Locate every Plasmodium falciparum-infected red blood cell.
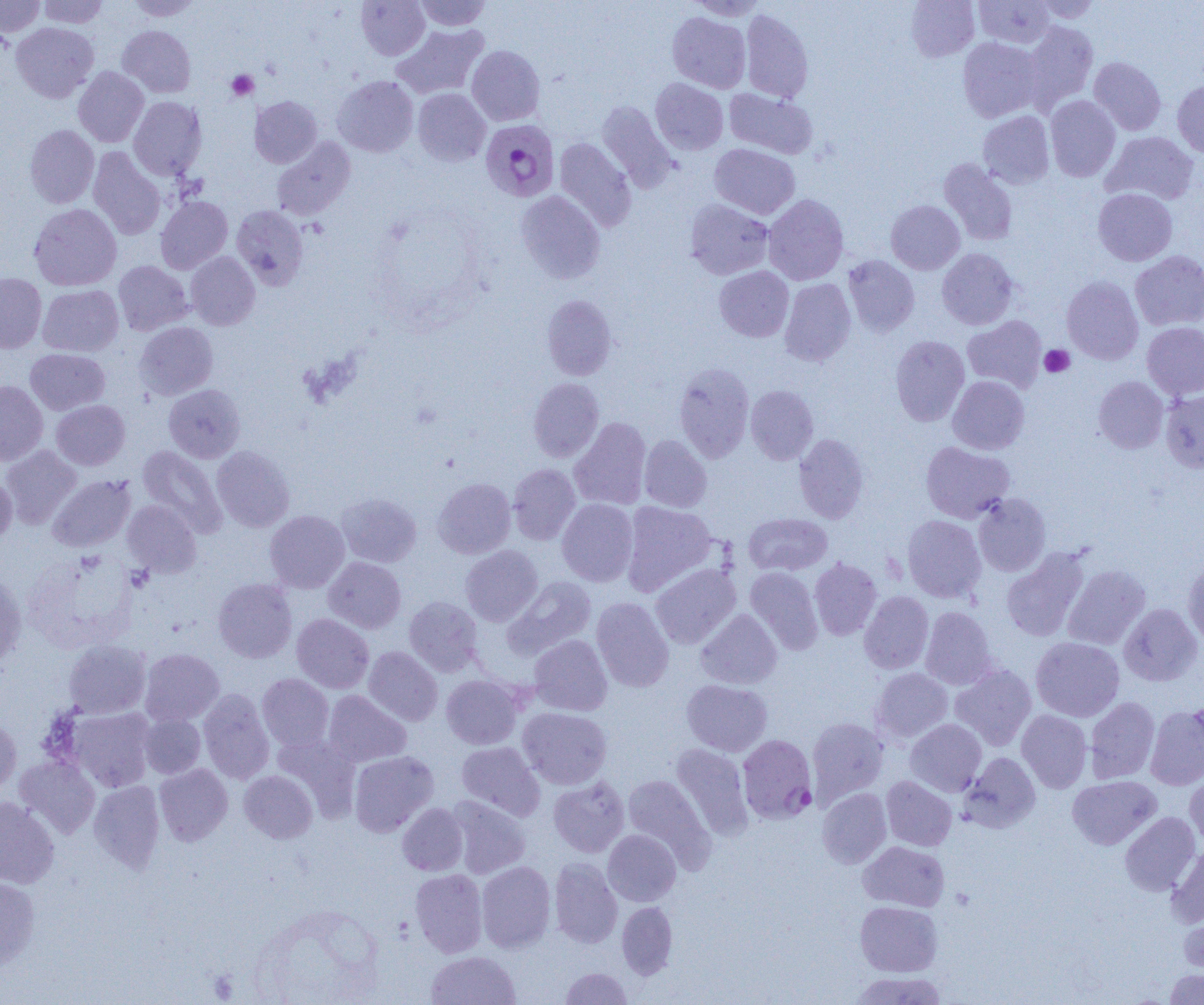
Approximate bounding boxes as (x1, y1, x2, y2) in pixels.
Plasmodium falciparum-infected red blood cells: (480, 119, 560, 202), (737, 734, 817, 824).

slide-level diagnosis = Plasmodium falciparum
modality = light microscopy
image size = 1204×1005 pixels
preparation = thin blood film
platelet locations = approximate bounding boxes as (x1, y1, x2, y2) in pixels: (226, 70, 258, 100), (1039, 344, 1074, 377)
field of view = one of a larger specimen
uninfected red blood cell locations = approximate bounding boxes as (x1, y1, x2, y2) in pixels: (0, 0, 45, 38), (37, 0, 109, 28), (125, 0, 203, 20), (356, 0, 430, 60), (414, 0, 492, 30), (687, 0, 768, 21), (906, 0, 979, 62), (974, 0, 1055, 48), (1032, 0, 1101, 23), (741, 9, 813, 103), (667, 12, 751, 93), (1023, 21, 1098, 110), (11, 22, 99, 103), (392, 23, 489, 99), (117, 25, 196, 97), (958, 37, 1043, 122), (466, 45, 545, 125), (1089, 57, 1166, 135), (73, 67, 149, 147), (331, 76, 419, 157), (650, 78, 728, 155), (1172, 80, 1204, 158), (412, 88, 491, 166), (724, 88, 818, 159), (1045, 95, 1120, 181), (128, 96, 207, 180), (250, 96, 322, 168), (596, 100, 677, 193), (978, 111, 1054, 189), (25, 125, 99, 208), (1102, 131, 1199, 205), (272, 137, 356, 221), (554, 137, 636, 232), (710, 143, 800, 219), (88, 147, 166, 240), (939, 158, 1018, 246), (1093, 188, 1177, 265), (515, 191, 605, 284), (763, 194, 849, 285), (155, 196, 232, 274), (685, 199, 774, 279), (886, 200, 965, 274), (29, 203, 121, 290), (231, 205, 308, 289), (937, 248, 1018, 330), (185, 251, 260, 330), (1130, 251, 1204, 331), (843, 255, 919, 336), (113, 260, 193, 335), (714, 266, 794, 342), (0, 274, 47, 353), (1062, 276, 1143, 365), (779, 278, 856, 366), (38, 285, 123, 356), (541, 294, 617, 380), (963, 315, 1047, 392), (134, 322, 218, 400), (1142, 322, 1204, 400), (890, 335, 970, 426), (25, 348, 110, 414), (674, 363, 755, 462), (948, 375, 1029, 454), (1093, 376, 1168, 453), (528, 378, 604, 462), (0, 381, 48, 465), (163, 384, 245, 463), (746, 385, 818, 465), (1161, 388, 1204, 473), (51, 400, 130, 470), (569, 417, 651, 510), (793, 434, 869, 523), (639, 435, 712, 512), (920, 441, 1015, 522), (1, 445, 81, 528), (137, 445, 227, 536), (212, 446, 295, 532), (508, 463, 581, 545), (0, 474, 16, 548), (47, 475, 136, 552), (432, 477, 516, 558), (336, 492, 421, 567), (973, 493, 1051, 576), (557, 499, 638, 586), (123, 500, 202, 578), (621, 501, 718, 596), (265, 510, 349, 593), (743, 513, 832, 575), (902, 515, 986, 602), (460, 545, 543, 625), (1001, 547, 1090, 642), (324, 557, 405, 633), (809, 557, 882, 640), (1183, 560, 1204, 648), (650, 563, 741, 649), (1062, 564, 1150, 650), (745, 567, 823, 655), (0, 569, 26, 668), (506, 576, 597, 657), (213, 578, 297, 663), (859, 591, 933, 674), (404, 596, 482, 676), (591, 597, 674, 692), (1119, 603, 1202, 686), (920, 606, 997, 690), (696, 609, 782, 689), (292, 613, 374, 693), (529, 635, 612, 716), (1031, 636, 1125, 721), (63, 640, 151, 719), (363, 646, 443, 726), (139, 649, 224, 726), (950, 664, 1037, 750), (870, 668, 953, 743), (257, 673, 334, 751), (441, 674, 524, 749), (681, 679, 772, 756), (198, 689, 274, 784), (324, 690, 411, 767), (1085, 696, 1159, 783), (1145, 704, 1204, 790), (69, 707, 155, 791), (518, 707, 612, 789), (1016, 709, 1092, 792), (139, 714, 205, 778), (807, 717, 889, 804), (0, 718, 21, 797), (905, 719, 986, 796), (273, 732, 361, 819), (456, 742, 545, 820), (671, 743, 753, 839), (349, 751, 438, 837), (960, 752, 1041, 833), (15, 755, 100, 838), (154, 763, 233, 845), (239, 770, 317, 843), (1185, 771, 1204, 848), (621, 774, 715, 868), (1067, 775, 1161, 849), (548, 776, 630, 857), (881, 776, 957, 851), (89, 781, 164, 872), (817, 788, 891, 868), (0, 796, 59, 888), (446, 796, 531, 879), (397, 802, 468, 875), (1120, 812, 1200, 895), (603, 829, 681, 906), (858, 841, 950, 911), (1166, 847, 1204, 927), (549, 857, 623, 948), (477, 861, 556, 953), (410, 868, 487, 957), (0, 876, 40, 971), (617, 901, 677, 978), (855, 901, 942, 976), (1179, 909, 1204, 976), (426, 951, 520, 1005), (559, 967, 633, 1004), (1164, 969, 1204, 1004), (850, 971, 949, 1004)
magnification = 1000x